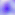
Summary:
  - Identification: Toxoplasma gondii
  - Magnification: 400x
  - Modality: photomicrograph